State which parasite is depicted.
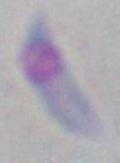

This is Toxoplasma gondii.

modality = photomicrograph
magnification = 1000x